Outline each blood parasite and name the species.
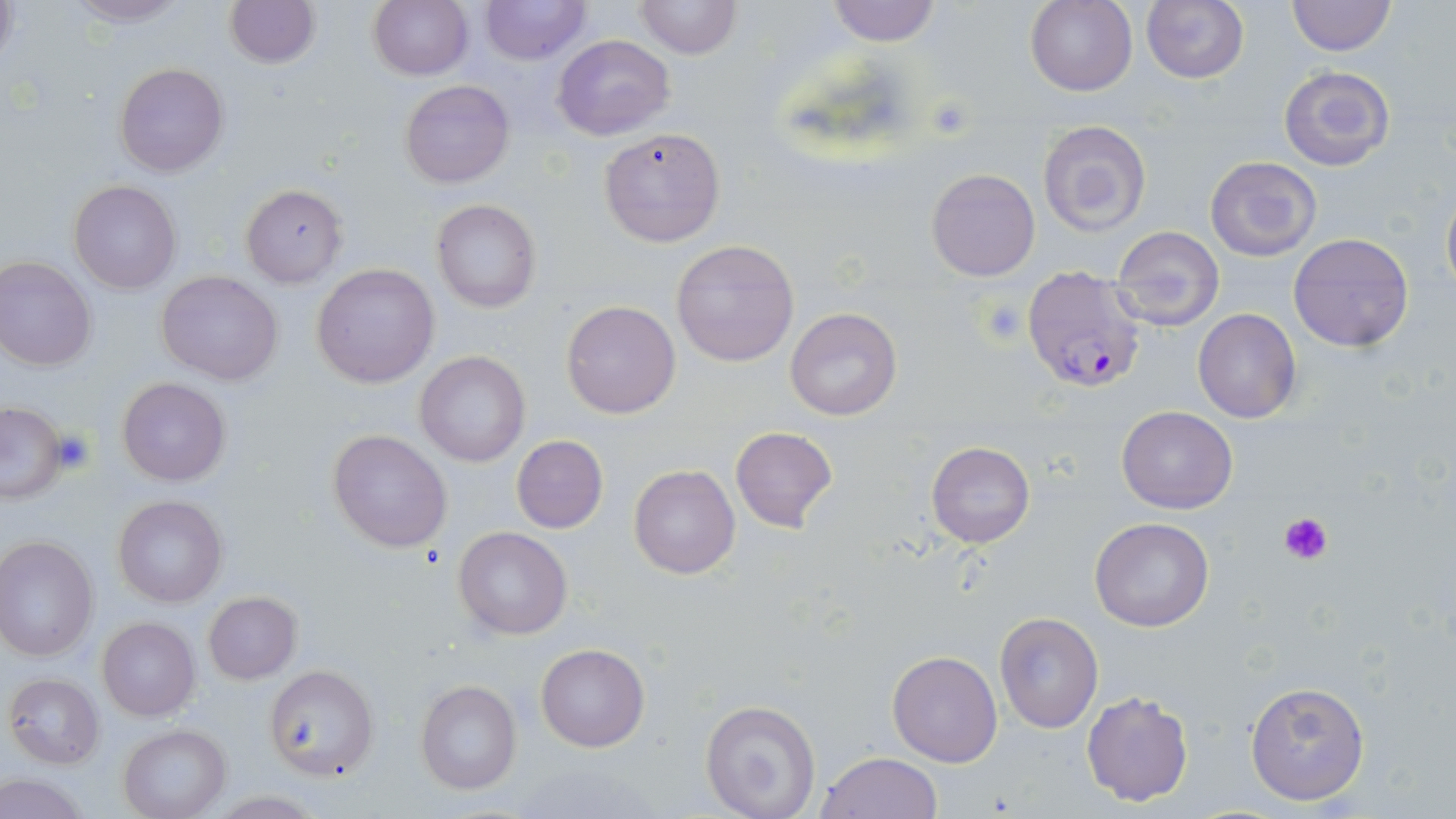
Approximate bounding boxes as (x1,y1)-(x2,y2) corner pairs in pixels.
Plasmodium falciparum-infected red blood cells: (1021,267)-(1145,393).
No Plasmodium ovale, Plasmodium malariae, Plasmodium vivax, Babesia divergens, or Trypanosoma brucei observed.

Summary:
  - Uninfected red blood cell locations: (0,0)-(20,71), (65,0)-(188,26), (223,0)-(319,68), (369,0)-(473,80), (479,0)-(590,66), (634,0)-(740,61), (826,0)-(943,46), (1026,0)-(1138,96), (1141,0)-(1250,85), (1287,0)-(1395,56), (552,33)-(675,140), (115,63)-(229,178), (1279,65)-(1394,171), (399,79)-(514,187), (1037,119)-(1152,237), (598,127)-(725,247), (1205,156)-(1321,260), (926,168)-(1040,281), (69,180)-(181,294), (241,183)-(348,288), (1441,185)-(1456,304), (431,199)-(541,313), (1111,226)-(1225,331), (1287,232)-(1414,353), (671,239)-(800,367), (0,255)-(98,370), (311,263)-(438,387), (157,271)-(283,385), (562,299)-(680,419), (784,308)-(903,422), (1193,309)-(1301,423), (416,352)-(531,464), (118,377)-(232,486), (0,402)-(67,504), (1116,406)-(1238,512), (730,426)-(838,532), (328,429)-(454,552), (512,435)-(608,533), (927,441)-(1034,549), (629,465)-(741,580), (113,495)-(228,608), (1088,516)-(1215,631), (454,527)-(571,640), (0,536)-(98,661), (202,592)-(302,684), (994,612)-(1104,733), (97,617)-(199,721), (536,643)-(650,752), (886,649)-(1002,767), (262,666)-(378,781), (4,674)-(104,768), (1244,678)-(1371,807), (415,680)-(522,796), (1080,688)-(1195,807), (699,700)-(822,819), (118,724)-(231,819), (816,750)-(944,818), (0,773)-(94,818)
  - Platelet locations: (50,429)-(99,475), (1280,512)-(1332,567)
  - Slide-level diagnosis: Plasmodium falciparum
  - Field of view: single
  - Image size: 1456×819 pixels
  - Stain: May-Grünwald-Giemsa
  - Modality: light microscopy
  - Preparation: thin blood smear
  - Magnification: 1000x